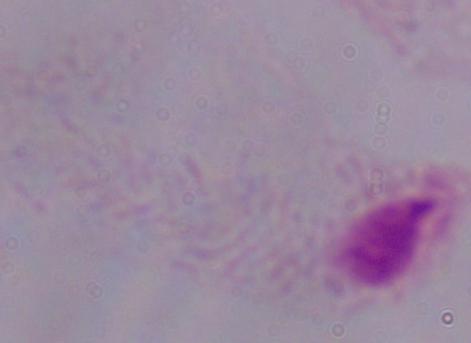
Micrograph. A trichomonad is shown. 1000x magnification.